Name the parasite shown.
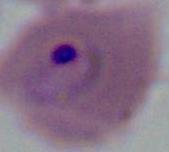

This is Plasmodium.

modality: micrograph
magnification: 400x or 1000x